Comment on the morphology of the erythrocytes.
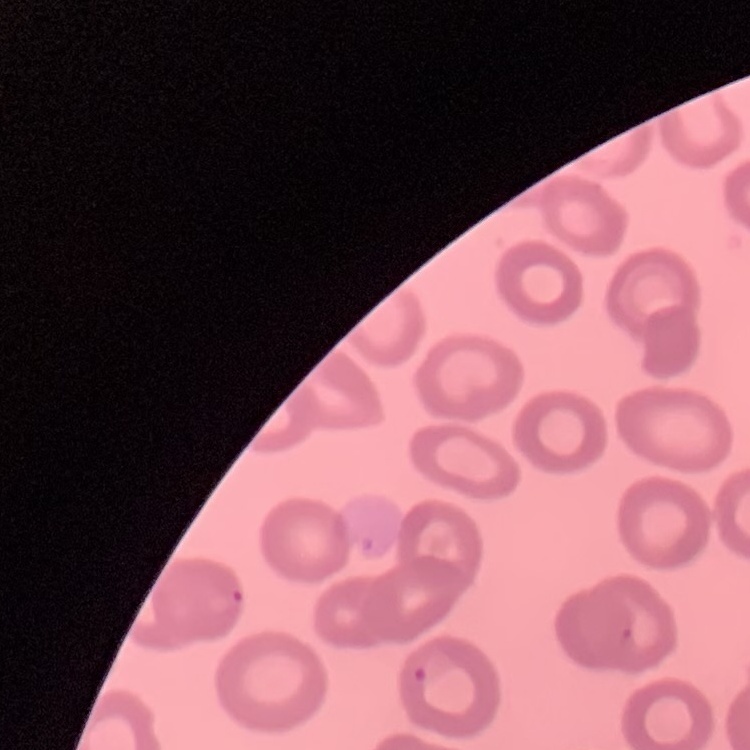
They show no rouleaux formation.

{
  "preparation": "thin blood smear",
  "stain": "Field's or Giemsa",
  "image_type": "one tile cut from a larger photomicrograph"
}